State the preparation type.
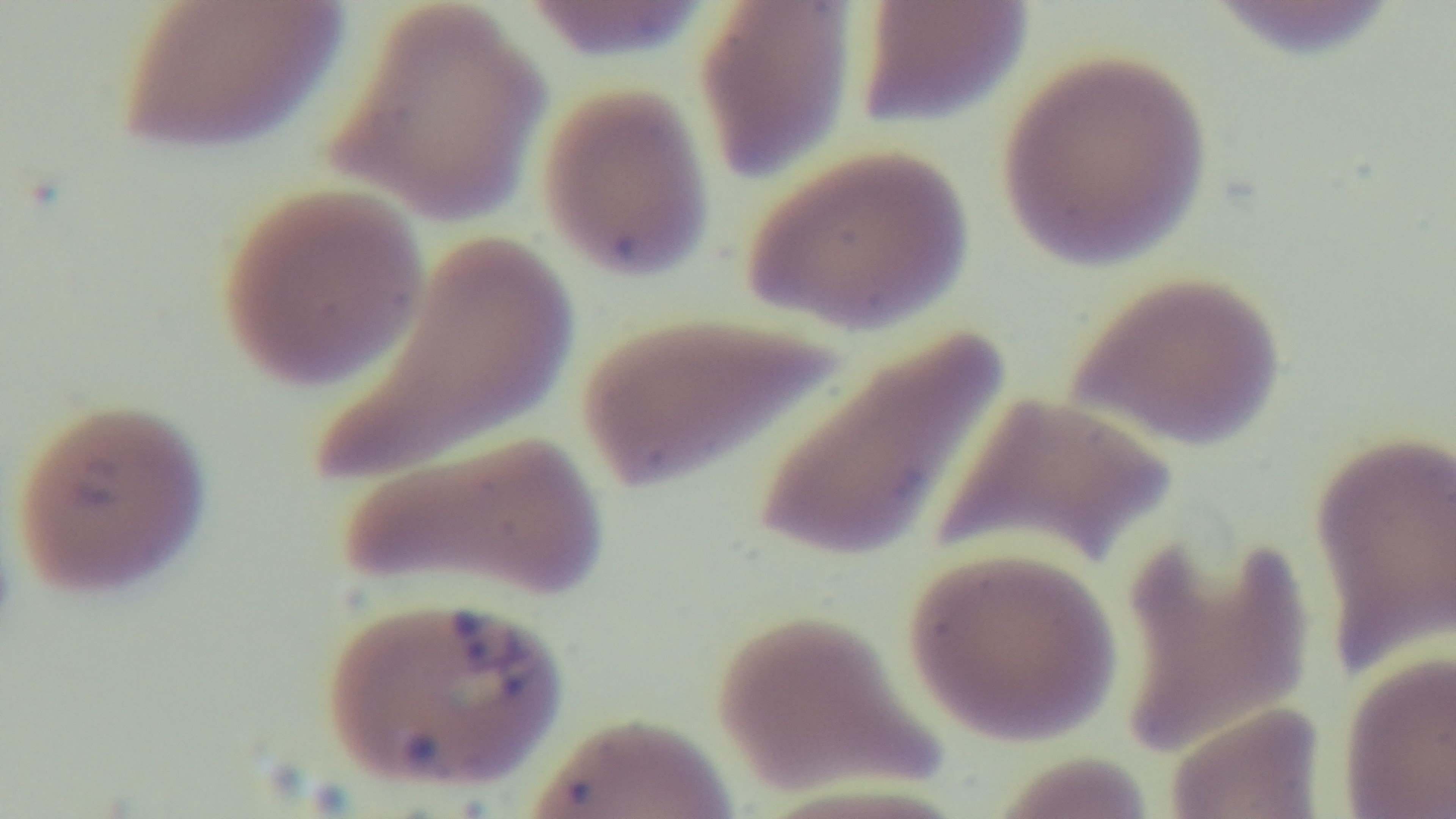

It is a thin blood film.

One field from the slide. Light microscopy. Captured with a mounted 4K digital camera. Malaria status: infected. 100x oil-immersion objective. Giemsa-stained.